Comment on the morphology of the red blood cells.
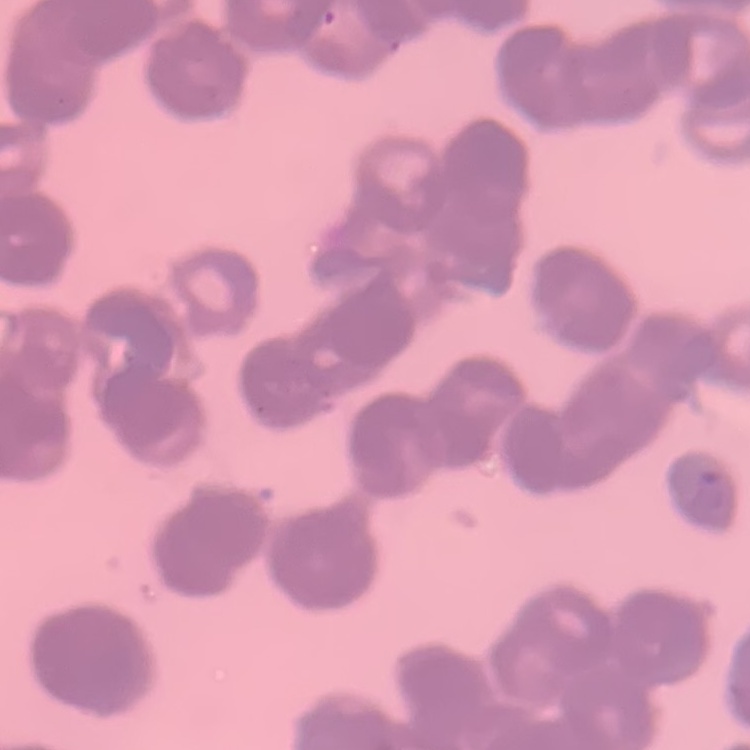
Rouleaux formation.

Field's or Giemsa stain. Square crop of a larger photomicrograph. Thin peripheral smear.